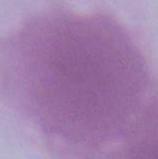 Captured at 1000x magnification. A red blood cell is shown. Photomicrograph.